Give the extent of all Plasmodium falciparum-infected red blood cells.
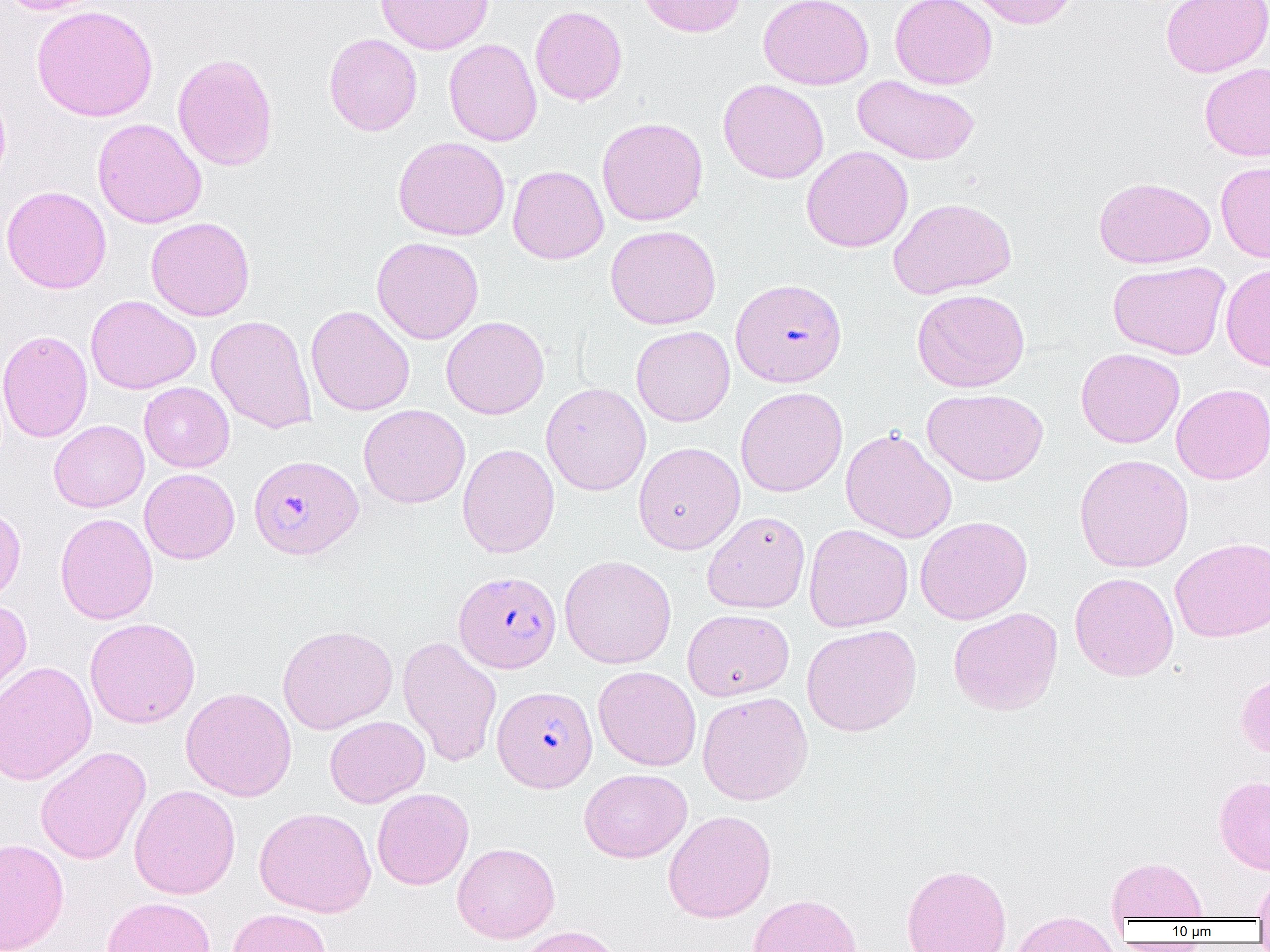
Approximate bounding boxes as [x1, y1, x2, y2] in pixels.
Plasmodium falciparum-infected red blood cells: [730, 278, 847, 387], [249, 454, 363, 560], [454, 570, 561, 673], [493, 685, 598, 792].

{
  "slide_level_diagnosis": "Plasmodium falciparum",
  "image_size": "1270×952 pixels",
  "magnification": "1000x",
  "field_of_view": "one of a larger specimen",
  "uninfected_red_blood_cell_locations": "approximate bounding boxes as [x1, y1, x2, y2] in pixels: [2, 0, 107, 14], [374, 0, 494, 55], [636, 0, 746, 37], [758, 0, 874, 90], [890, 0, 997, 89], [964, 0, 1079, 29], [1160, 0, 1270, 77], [31, 4, 158, 122], [530, 5, 628, 106], [323, 33, 422, 136], [444, 38, 542, 146], [172, 53, 278, 172], [1199, 62, 1270, 161], [851, 75, 981, 166], [718, 79, 829, 184], [0, 85, 11, 191], [596, 117, 708, 226], [92, 118, 207, 229], [393, 137, 510, 241], [801, 146, 913, 253], [1216, 160, 1270, 263], [508, 165, 609, 264], [1094, 176, 1216, 268], [1, 185, 111, 294], [888, 197, 1017, 299], [146, 217, 255, 321], [605, 225, 721, 330], [372, 236, 483, 344], [1108, 260, 1231, 360], [1220, 263, 1270, 370], [912, 288, 1030, 393], [85, 295, 201, 394], [306, 305, 415, 416], [206, 315, 317, 434], [441, 316, 549, 419], [631, 325, 735, 426], [0, 329, 93, 443], [1075, 348, 1185, 448], [139, 382, 234, 472], [541, 382, 651, 495], [1171, 383, 1270, 485], [735, 386, 847, 497], [922, 388, 1048, 485], [358, 404, 470, 509], [49, 420, 149, 512], [840, 428, 958, 544], [633, 441, 745, 554], [457, 443, 560, 558], [1073, 454, 1194, 573], [139, 468, 240, 564], [0, 505, 26, 608], [702, 510, 810, 613], [55, 513, 158, 625], [915, 516, 1033, 625], [804, 523, 913, 632], [1169, 537, 1270, 642], [559, 554, 677, 669], [1069, 572, 1179, 681], [0, 599, 32, 706], [947, 607, 1063, 716], [682, 608, 794, 701], [84, 617, 201, 729], [277, 624, 397, 734], [801, 624, 922, 737], [397, 636, 502, 768], [0, 660, 97, 786], [593, 666, 701, 771], [1235, 670, 1270, 760], [180, 687, 297, 801], [696, 691, 813, 805], [324, 715, 430, 808], [35, 746, 151, 864], [579, 768, 692, 862], [1214, 775, 1270, 874], [129, 784, 241, 899], [372, 788, 474, 890], [254, 806, 376, 917], [663, 809, 776, 922], [0, 838, 69, 952], [452, 842, 560, 943], [1107, 856, 1208, 922], [901, 863, 1012, 952], [1254, 872, 1270, 920], [748, 893, 862, 952], [100, 896, 217, 952], [227, 908, 332, 952], [1010, 911, 1120, 952], [515, 925, 625, 952]",
  "preparation": "thin blood film",
  "modality": "optical microscopy"
}